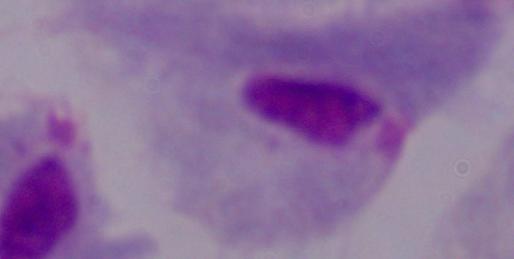
Micrograph. 1000x magnification. A trichomonad is shown.